Name the parasite shown.
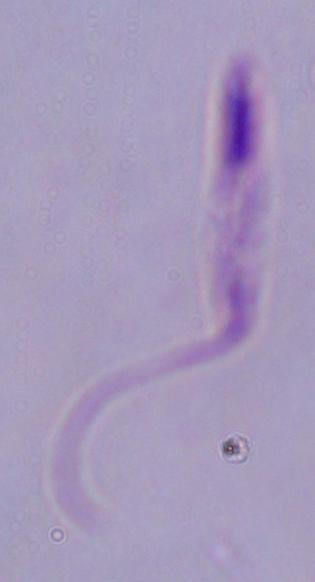
Leishmania.

Summary:
  - Modality: photomicrograph
  - Magnification: 1000x